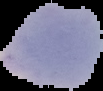

Summary:
  - Malaria status: parasitized
  - Preparation: thin blood film
  - Image size: 103×91 pixels
  - Image type: segmented cell region on a black background